Assess this cell for malaria.
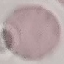
It is uninfected.

Cell patch, automatically extracted from a larger field of view and resized to 64 × 64 pixels. Giemsa-stained preparation. Photographed with a smartphone camera at the microscope eyepiece. Thin blood smear.